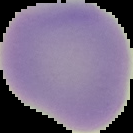

Result: negative for malaria parasites. Image is 133×133 pixels. The area outside the segmented cell region is set to black. From a thin blood smear.